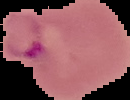

From a thin blood film. Image is 130×100 pixels. Segmented cell region on a black background. Result: malaria parasites identified.